State the blood parasite species.
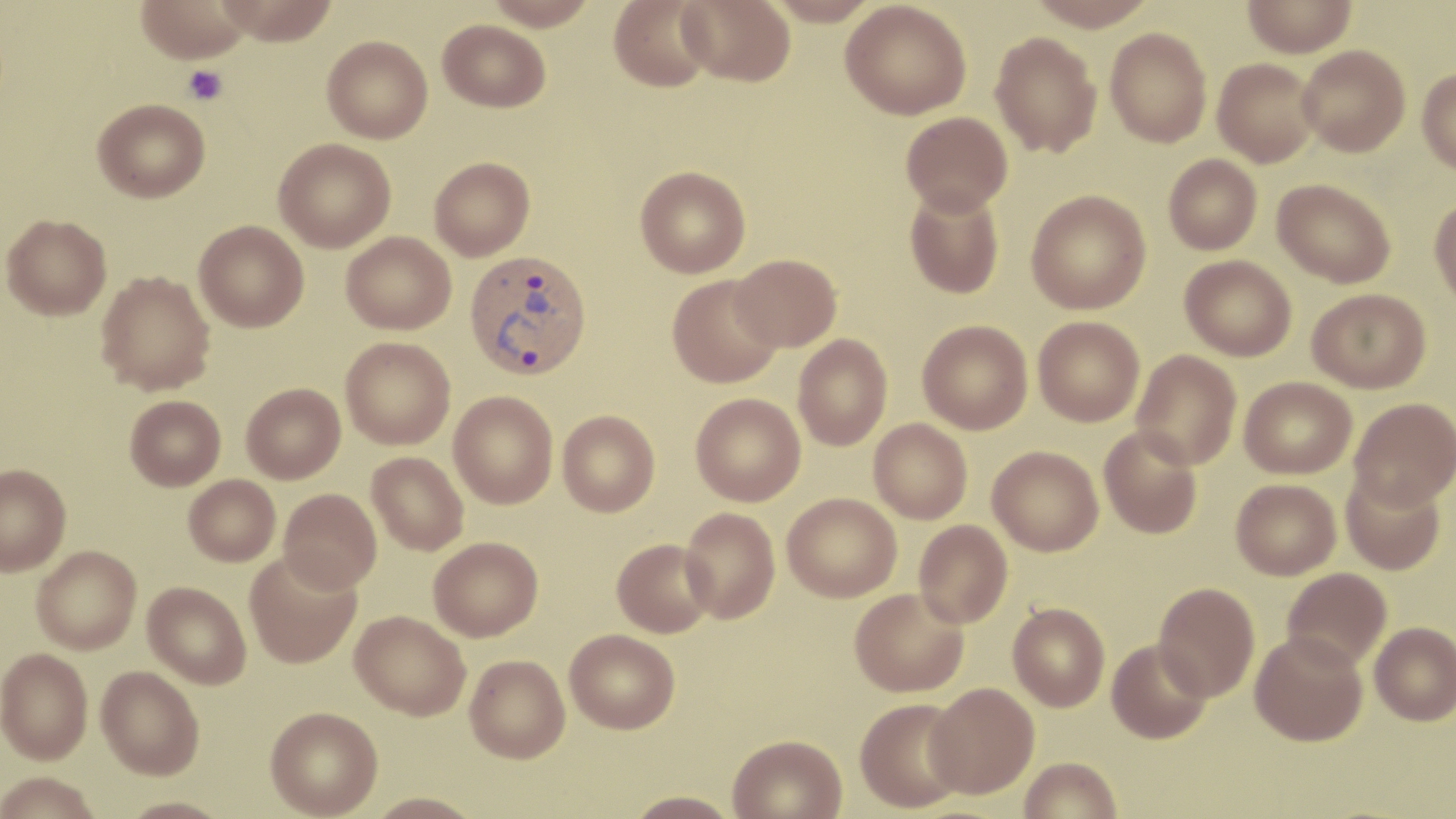
Plasmodium vivax.

Approximate bounding boxes as (x1, y1, x2, y2) in pixels. Platelet locations: (183, 65, 229, 106). Plasmodium vivax-infected red blood cell locations: (464, 248, 593, 381). Uninfected red blood cell locations: (135, 0, 253, 63), (216, 0, 339, 45), (483, 0, 600, 30), (609, 0, 715, 92), (677, 0, 795, 86), (766, 0, 881, 26), (1025, 0, 1158, 31), (1243, 0, 1358, 57), (841, 1, 971, 120), (438, 19, 551, 112), (1105, 27, 1212, 147), (990, 31, 1102, 158), (322, 35, 432, 143), (1297, 45, 1410, 157), (1213, 58, 1321, 167), (1417, 68, 1456, 174), (93, 98, 210, 202), (900, 111, 1013, 215), (273, 138, 396, 252), (1163, 154, 1262, 254), (429, 157, 535, 261), (635, 165, 751, 277), (1272, 178, 1396, 288), (904, 186, 1005, 299), (1026, 189, 1151, 314), (1429, 197, 1456, 308), (1, 213, 112, 320), (194, 220, 309, 332), (341, 231, 457, 334), (731, 253, 842, 351), (1180, 255, 1296, 361), (96, 270, 216, 395), (667, 274, 783, 388), (1307, 288, 1431, 393), (1033, 315, 1144, 426), (917, 320, 1033, 435), (793, 334, 892, 450), (340, 337, 456, 449), (1131, 350, 1241, 470), (1240, 376, 1357, 479), (241, 382, 346, 483), (449, 391, 558, 509), (690, 393, 805, 506), (124, 395, 226, 490), (1348, 398, 1456, 510), (557, 410, 661, 517), (869, 418, 972, 523), (1099, 426, 1203, 539), (987, 446, 1104, 556), (366, 452, 469, 555), (0, 464, 71, 576), (1341, 469, 1446, 575), (183, 474, 280, 566), (1231, 478, 1341, 580), (278, 489, 381, 593), (782, 492, 902, 602), (679, 507, 780, 624), (914, 520, 1013, 629), (428, 536, 543, 641), (612, 538, 716, 638), (31, 545, 141, 655), (245, 550, 362, 669), (1282, 567, 1392, 672), (142, 581, 251, 689), (1154, 582, 1260, 702), (849, 587, 969, 697), (1008, 602, 1110, 712), (350, 610, 471, 721), (1370, 621, 1456, 725), (565, 629, 680, 734), (1249, 630, 1368, 746), (1107, 639, 1211, 744), (0, 649, 92, 766), (465, 654, 570, 763), (96, 667, 204, 781), (925, 683, 1039, 799), (855, 698, 969, 814), (265, 707, 383, 818), (727, 733, 848, 819), (1019, 756, 1122, 819), (0, 775, 101, 819), (624, 789, 742, 818), (364, 792, 483, 818), (120, 798, 231, 819). Image is 1456×819 pixels. Thin blood film. Captured at 1000x magnification. May-Grünwald-Giemsa stain. Light microscopy. One field of a larger specimen.